Assess this cell for malaria.
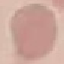

Uninfected.

image type = cell patch, automatically extracted from a larger field of view and resized to 64 × 64 pixels
stain = Giemsa
capture = smartphone camera at the microscope eyepiece
preparation = thin blood smear